Classify this cell by malaria status.
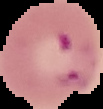
Parasitized.

Cell region segmented out of the field of view; the surrounding area is masked to black. Image is 103×109 pixels. From a thin blood smear.